Name the blood parasite species.
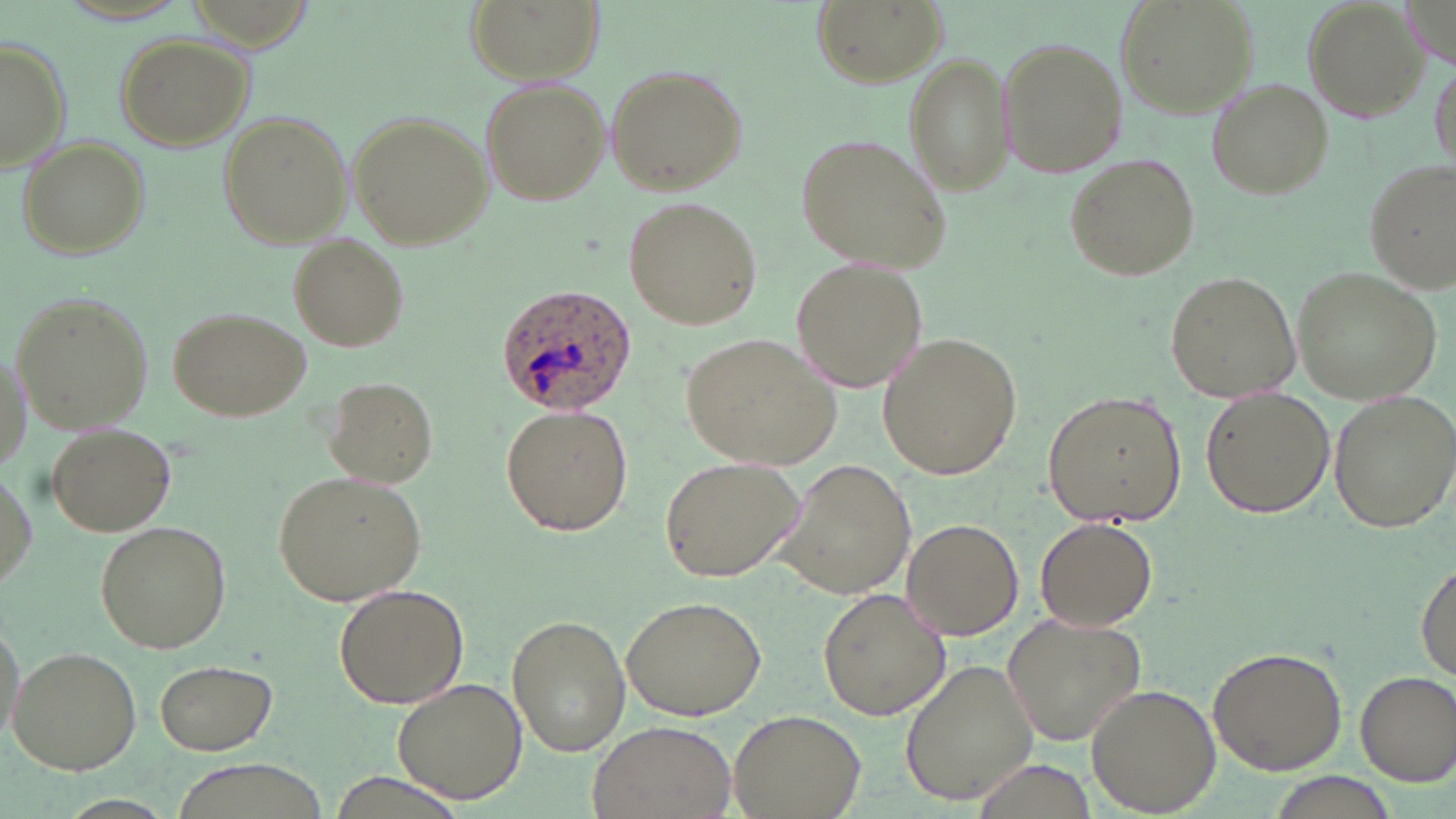
Plasmodium ovale.

Approximate bounding boxes as named x1/y1/x2/y2 corners in pixels. Uninfected red blood cell locations: (x1=466, y1=0, x2=602, y2=87), (x1=1114, y1=0, x2=1259, y2=114), (x1=1303, y1=0, x2=1429, y2=120), (x1=815, y1=1, x2=947, y2=86), (x1=113, y1=33, x2=253, y2=151), (x1=0, y1=36, x2=71, y2=172), (x1=998, y1=36, x2=1127, y2=180), (x1=904, y1=54, x2=1014, y2=197), (x1=1429, y1=55, x2=1454, y2=173), (x1=603, y1=61, x2=746, y2=194), (x1=479, y1=77, x2=610, y2=204), (x1=1206, y1=78, x2=1333, y2=199), (x1=220, y1=111, x2=352, y2=248), (x1=346, y1=113, x2=491, y2=251), (x1=794, y1=132, x2=954, y2=275), (x1=15, y1=135, x2=149, y2=259), (x1=1067, y1=155, x2=1197, y2=282), (x1=1363, y1=159, x2=1453, y2=292), (x1=624, y1=197, x2=764, y2=329), (x1=289, y1=236, x2=411, y2=351), (x1=794, y1=257, x2=929, y2=393), (x1=1293, y1=269, x2=1441, y2=406), (x1=1163, y1=271, x2=1301, y2=402), (x1=10, y1=291, x2=154, y2=435), (x1=169, y1=308, x2=311, y2=421), (x1=878, y1=330, x2=1025, y2=480), (x1=680, y1=331, x2=841, y2=469), (x1=0, y1=344, x2=32, y2=479), (x1=326, y1=377, x2=441, y2=487), (x1=1042, y1=389, x2=1186, y2=530), (x1=1200, y1=389, x2=1334, y2=519), (x1=1329, y1=390, x2=1456, y2=533), (x1=501, y1=404, x2=633, y2=538), (x1=43, y1=420, x2=176, y2=536), (x1=659, y1=456, x2=806, y2=582), (x1=773, y1=458, x2=918, y2=598), (x1=0, y1=464, x2=37, y2=597), (x1=273, y1=470, x2=427, y2=608), (x1=902, y1=518, x2=1024, y2=641), (x1=1035, y1=518, x2=1157, y2=632), (x1=93, y1=519, x2=231, y2=654), (x1=1416, y1=559, x2=1455, y2=680), (x1=332, y1=582, x2=469, y2=708), (x1=818, y1=585, x2=951, y2=720), (x1=622, y1=595, x2=767, y2=721), (x1=0, y1=614, x2=25, y2=747), (x1=507, y1=614, x2=631, y2=756), (x1=999, y1=615, x2=1145, y2=744), (x1=8, y1=645, x2=143, y2=774), (x1=1207, y1=646, x2=1348, y2=774), (x1=153, y1=658, x2=280, y2=755), (x1=901, y1=658, x2=1039, y2=809), (x1=1355, y1=668, x2=1456, y2=784), (x1=393, y1=678, x2=527, y2=805), (x1=1086, y1=683, x2=1221, y2=814), (x1=729, y1=708, x2=864, y2=819), (x1=586, y1=720, x2=738, y2=819). Plasmodium ovale-infected red blood cell locations: (x1=495, y1=283, x2=636, y2=415). 1000x magnification. Image is 1456×819 pixels. Light microscopy. May-Grünwald-Giemsa-stained preparation. Single field of view. Thin blood film.